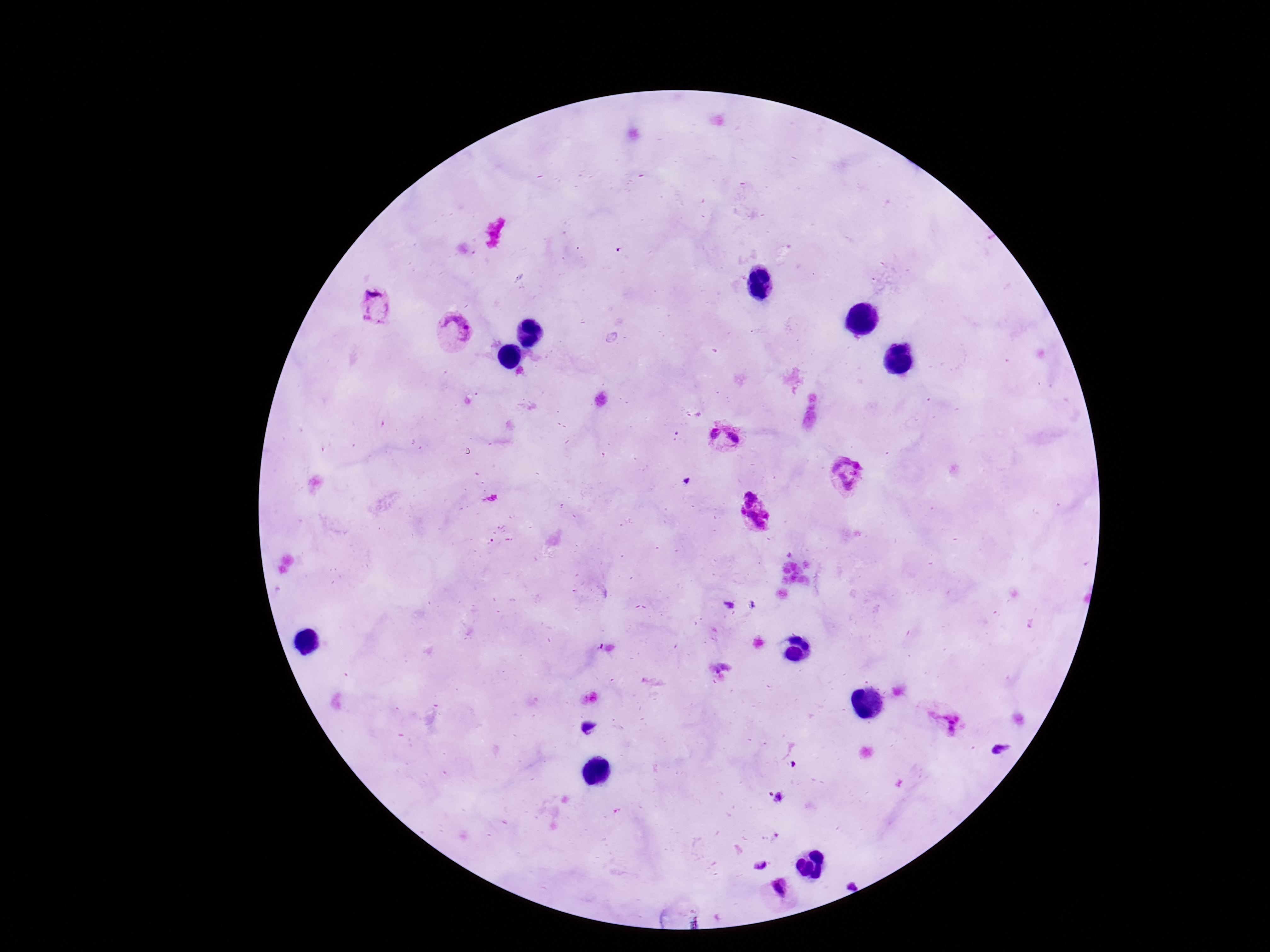

{
  "preparation": "thick blood film",
  "field_of_view": "single",
  "plasmodium_parasite_locations": "approximate centers as (x, y) in pixels: (374, 305), (455, 330), (726, 437), (843, 471), (754, 513), (942, 719), (587, 728), (779, 798), (760, 865), (779, 892)",
  "capture": "smartphone camera through the microscope eyepiece",
  "magnification": "100x",
  "patient_malaria_status": "infected",
  "stain": "Giemsa",
  "image_size": "1270×952 pixels"
}